Assess this cell for malaria.
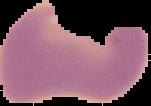

Uninfected.

From a thin blood smear. Cell region segmented out of the field of view; the surrounding area is masked to black. Image is 151×106 pixels.